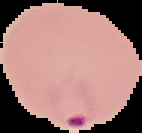

Summary:
  - Malaria status: parasitized
  - Image type: segmented cell region on a black background
  - Image size: 142×133 pixels
  - Preparation: thin blood smear